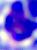

Summary:
  - Identification: leukocyte
  - Magnification: 400x
  - Modality: micrograph